Classify the preparation.
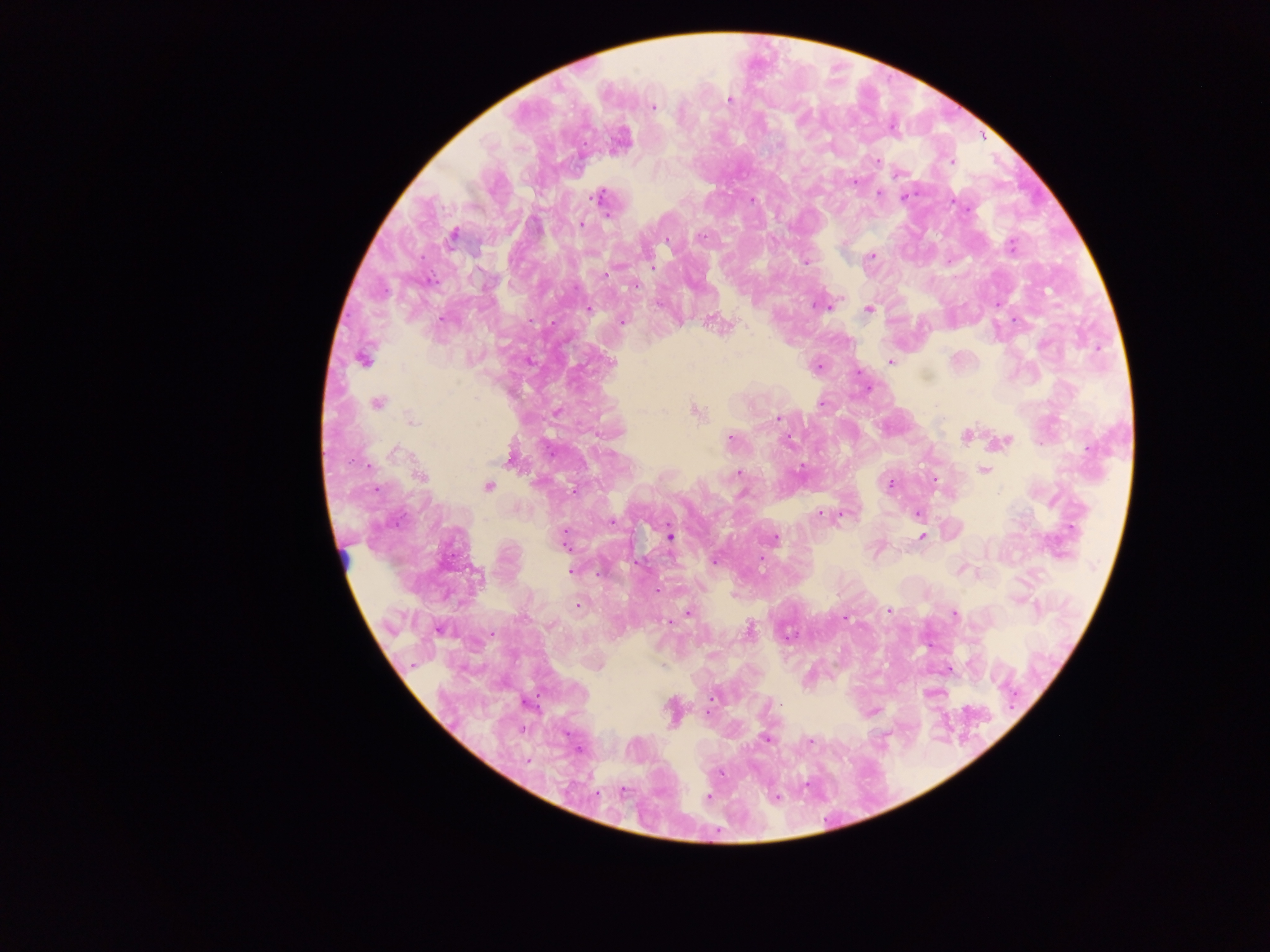

Thick blood smear.

Approximate centers as (x, y) in pixels.
Summary:
  - Plasmodium parasite locations: (730, 100), (653, 107), (778, 144), (877, 160), (952, 161), (855, 183), (878, 193), (597, 197), (905, 197), (752, 201), (968, 210), (581, 224), (453, 235), (703, 236), (667, 241), (1012, 246), (872, 256), (807, 262), (653, 267), (605, 275), (636, 286), (657, 305), (831, 305), (816, 306), (824, 307), (589, 309), (869, 309), (441, 319), (1015, 320), (621, 322), (714, 323), (362, 359), (890, 362), (611, 363), (818, 366), (377, 403), (822, 404), (696, 412), (778, 419), (412, 420), (966, 436), (730, 438), (788, 440), (1005, 441), (395, 452), (801, 469), (983, 470), (739, 473), (421, 477), (934, 479), (890, 485), (489, 486), (574, 490), (918, 513), (820, 514), (840, 515), (611, 523), (670, 536), (922, 536), (775, 538), (564, 539), (715, 560), (571, 571), (657, 590), (579, 605), (889, 610), (688, 612), (955, 614), (844, 618), (668, 622), (749, 629), (712, 698), (765, 739), (810, 741), (709, 797), (775, 797)
  - Country: Ghana
  - Field of view: single
  - Image size: 1270×952 pixels
  - Capture: mobile-phone photograph through a microscope